Name the parasite shown.
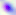

Toxoplasma gondii.

Summary:
  - Modality: micrograph
  - Magnification: 400x